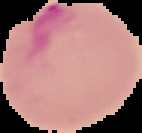
Summary:
  - Preparation: thin blood film
  - Malaria status: parasitized
  - Image type: segmented cell region on a black background
  - Image size: 142×133 pixels